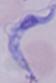

identification: trypanosome
magnification: 1000x
modality: micrograph